Report the malaria status of this cell.
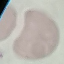

Uninfected.

Acquired by smartphone through the microscope eyepiece. Giemsa stain. Cell patch, automatically extracted from a larger field of view and resized to 64 × 64 pixels. Thin smear of blood.